Report the malaria status of this cell.
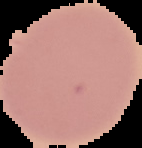
Uninfected.

preparation: thin blood smear
image_size: 142×148 pixels
image_type: segmented cell region on a black background